Identify the parasite.
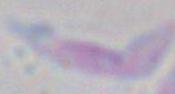

Toxoplasma gondii.

1000x magnification. Micrograph.